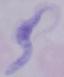
Summary:
  - Modality: photomicrograph
  - Magnification: 1000x
  - Identification: trypanosome